Report the malaria status of this cell.
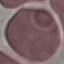
Uninfected.

Photographed with a smartphone camera at the microscope eyepiece. Thin blood smear. Giemsa stain. Automatically extracted cell patch, resized to 64 × 64 pixels.